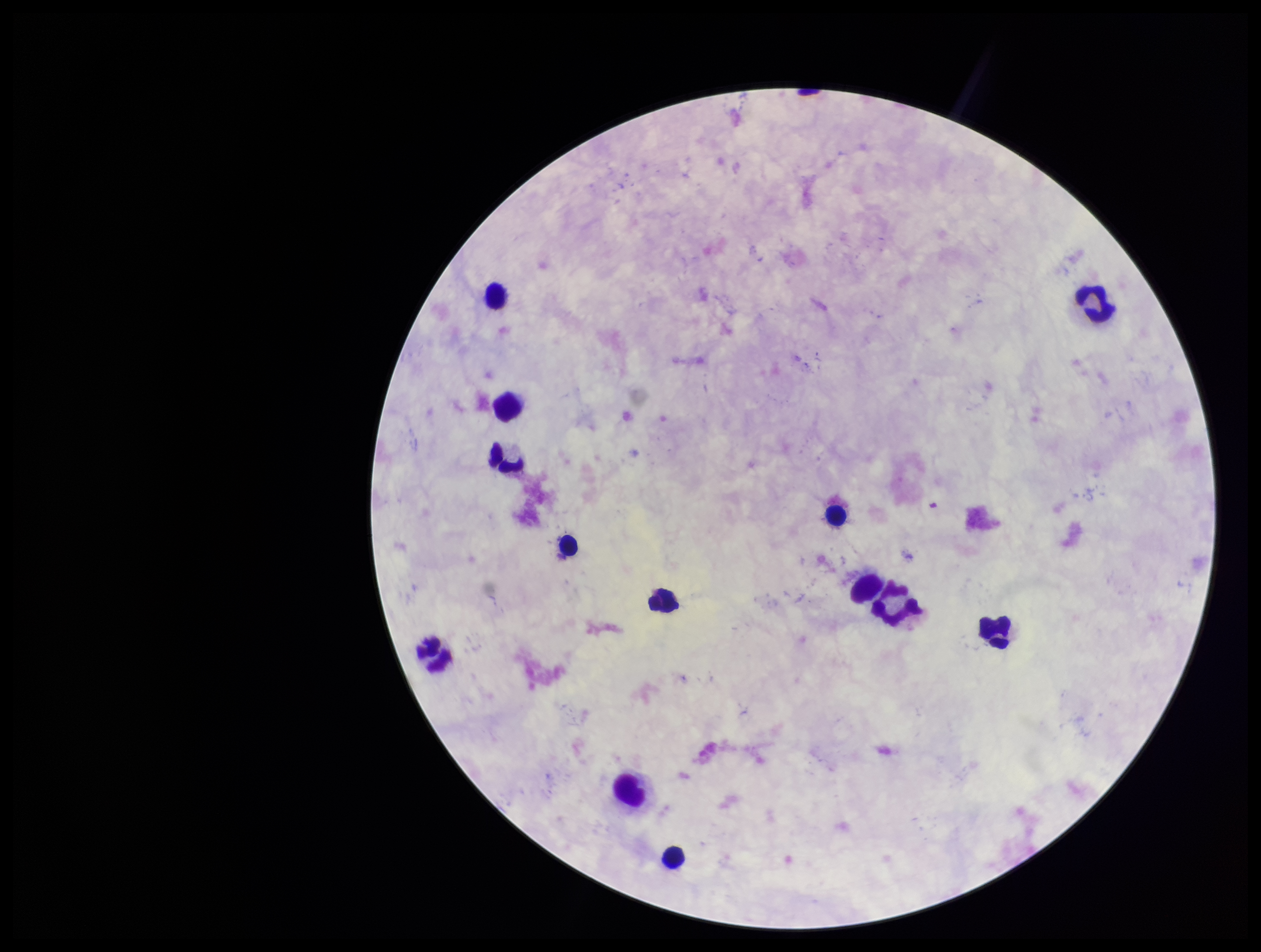

Patient malaria status: negative. Parasite count: 0. Leukocyte count: 13. Smartphone photograph taken through the eyepiece of a microscope. Plasmodium parasites: none identified. Stained with Giemsa. Image is 1261×952 pixels. Single field of view. Preparation: thick smear.